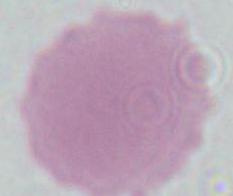

magnification = 1000x
modality = micrograph
identification = erythrocyte